Point out each Plasmodium parasite.
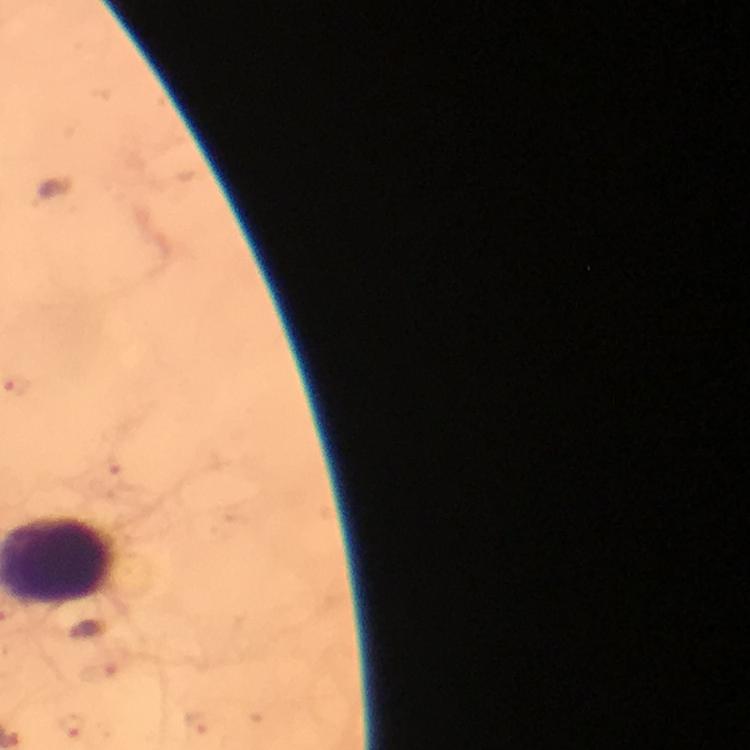
Approximate centers as (x, y) in pixels.
Plasmodium parasites: (100, 669), (199, 724), (73, 726).

Summary:
  - Immersion oil: used
  - Image size: 750×750 pixels
  - Capture: smartphone mounted on the microscope
  - Preparation: thick blood film
  - Context: from a diagnostic examination for malaria
  - Magnification: 100x
  - Cropped from: one field of view
  - Stain: Giemsa